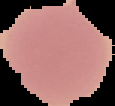
{
  "preparation": "thin blood film",
  "result": "no malaria parasites detected",
  "image_type": "segmented cell region on a black background",
  "image_size": "115×106 pixels"
}